Give the extent of all Plasmodium malariae-infected red blood cells.
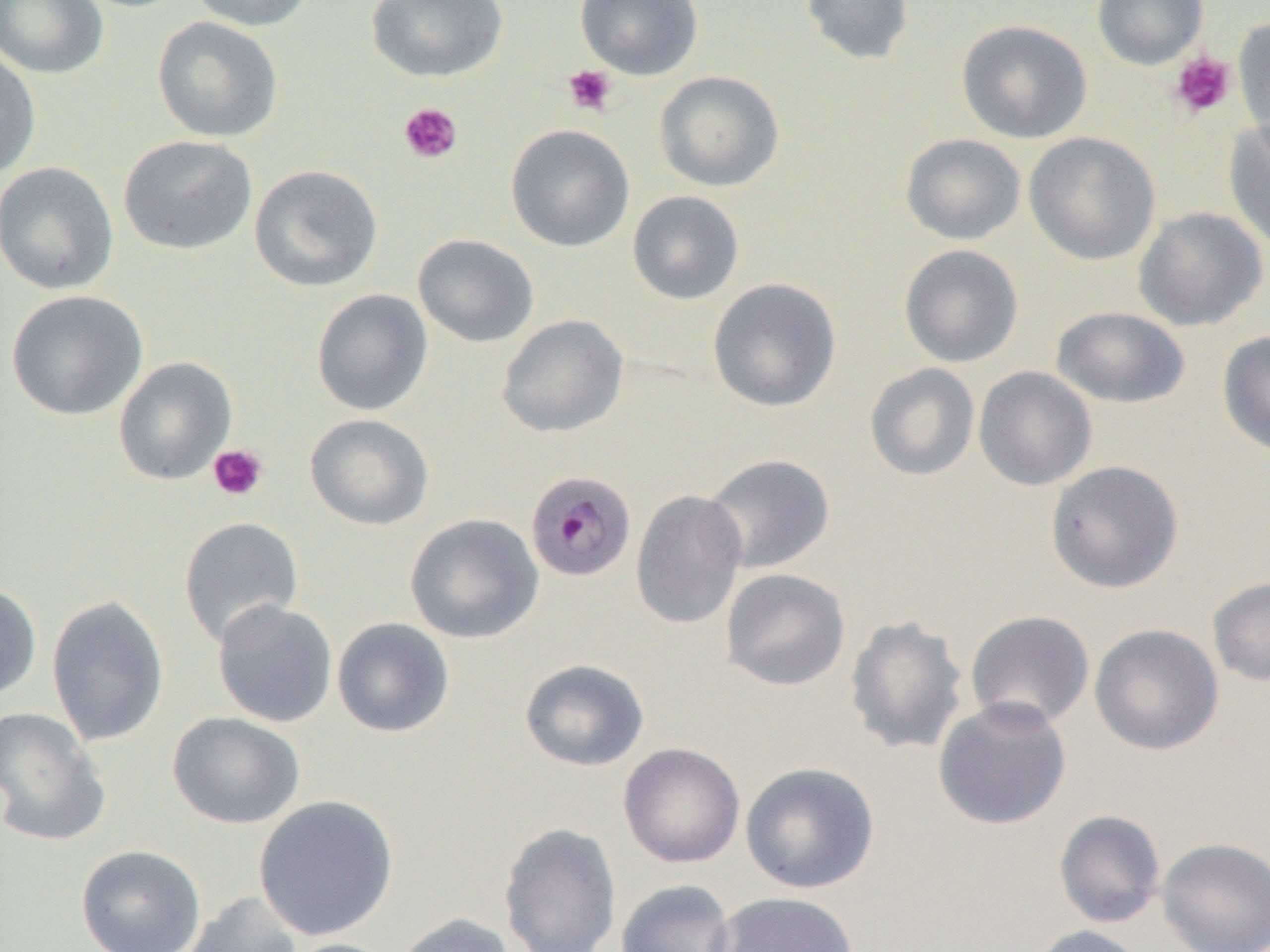
Approximate bounding boxes as (x1, y1, x2, y2) in pixels.
Plasmodium malariae-infected red blood cells: (525, 470, 637, 582).

slide-level diagnosis = Plasmodium malariae
field of view = one of a larger specimen
image size = 1270×952 pixels
preparation = thin blood smear
platelet locations (subset) = approximate bounding boxes as (x1, y1, x2, y2) in pixels: (1169, 51, 1236, 118), (562, 64, 617, 116), (399, 103, 462, 164), (208, 444, 269, 501)
magnification = 1000x
modality = optical microscopy
uninfected red blood cell locations (subset) = approximate bounding boxes as (x1, y1, x2, y2) in pixels: (187, 0, 316, 32), (366, 0, 508, 83), (575, 0, 703, 80), (800, 0, 914, 66), (1092, 0, 1208, 69), (0, 1, 109, 79), (152, 16, 284, 143), (1233, 16, 1270, 146), (956, 19, 1092, 144), (0, 47, 42, 180), (653, 70, 784, 192), (1224, 119, 1270, 254), (505, 124, 635, 252), (1023, 132, 1161, 266), (900, 133, 1026, 245), (118, 135, 258, 255), (0, 161, 119, 295), (249, 164, 383, 292), (627, 190, 744, 305), (1133, 206, 1268, 332), (412, 233, 539, 348), (899, 244, 1023, 367), (707, 277, 842, 413), (311, 288, 433, 416), (5, 289, 148, 421), (1051, 306, 1190, 409), (496, 314, 629, 438), (1217, 329, 1270, 456), (865, 363, 980, 481), (973, 366, 1097, 491), (304, 413, 434, 531), (701, 453, 836, 574), (1046, 460, 1184, 593), (630, 489, 748, 630), (405, 513, 544, 644), (178, 516, 304, 648), (721, 568, 850, 690), (1207, 576, 1270, 687), (0, 581, 42, 700), (47, 594, 169, 747), (211, 600, 338, 728), (964, 610, 1095, 731), (845, 614, 969, 755), (332, 617, 455, 738), (1089, 623, 1224, 756), (519, 659, 649, 772), (932, 697, 1072, 830), (0, 706, 111, 847), (167, 711, 306, 830), (618, 742, 745, 869), (741, 761, 880, 894), (253, 795, 399, 941), (1054, 810, 1166, 929), (498, 821, 622, 952), (1156, 837, 1270, 952), (75, 844, 206, 952), (615, 879, 736, 952), (180, 891, 303, 952), (707, 891, 859, 952), (396, 912, 519, 952), (1025, 924, 1150, 952), (278, 938, 406, 952)